Identify the preparation type.
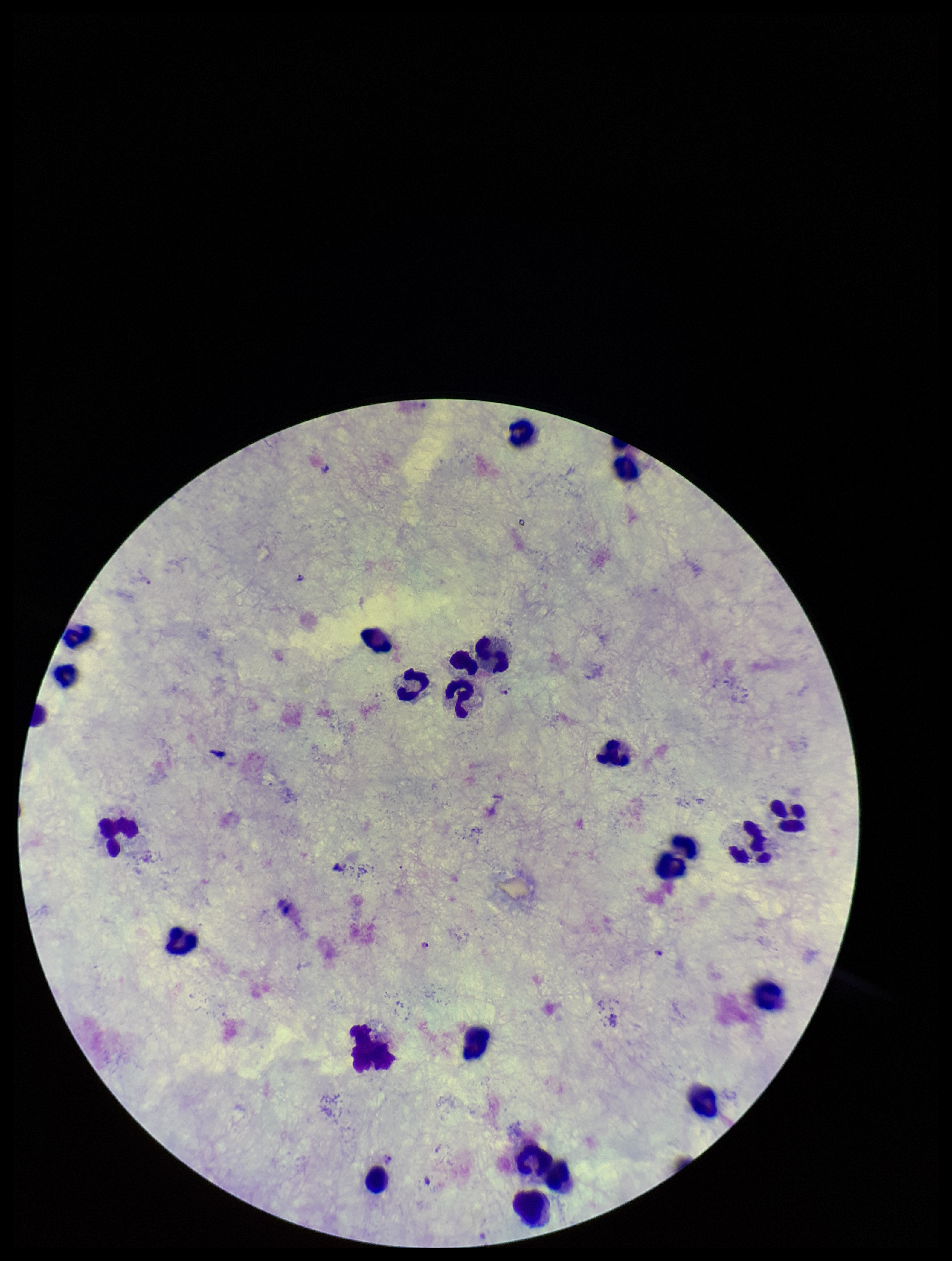
A thick smear.

parasite count = 7
leukocyte count = 25
capture = smartphone photograph through the microscope eyepiece
species reported for this patient = Plasmodium vivax
patient malaria status = infected
field of view = one from this slide
stain = Giemsa
Plasmodium parasites = seen
image size = 952×1261 pixels